Locate every blood parasite and identify its species.
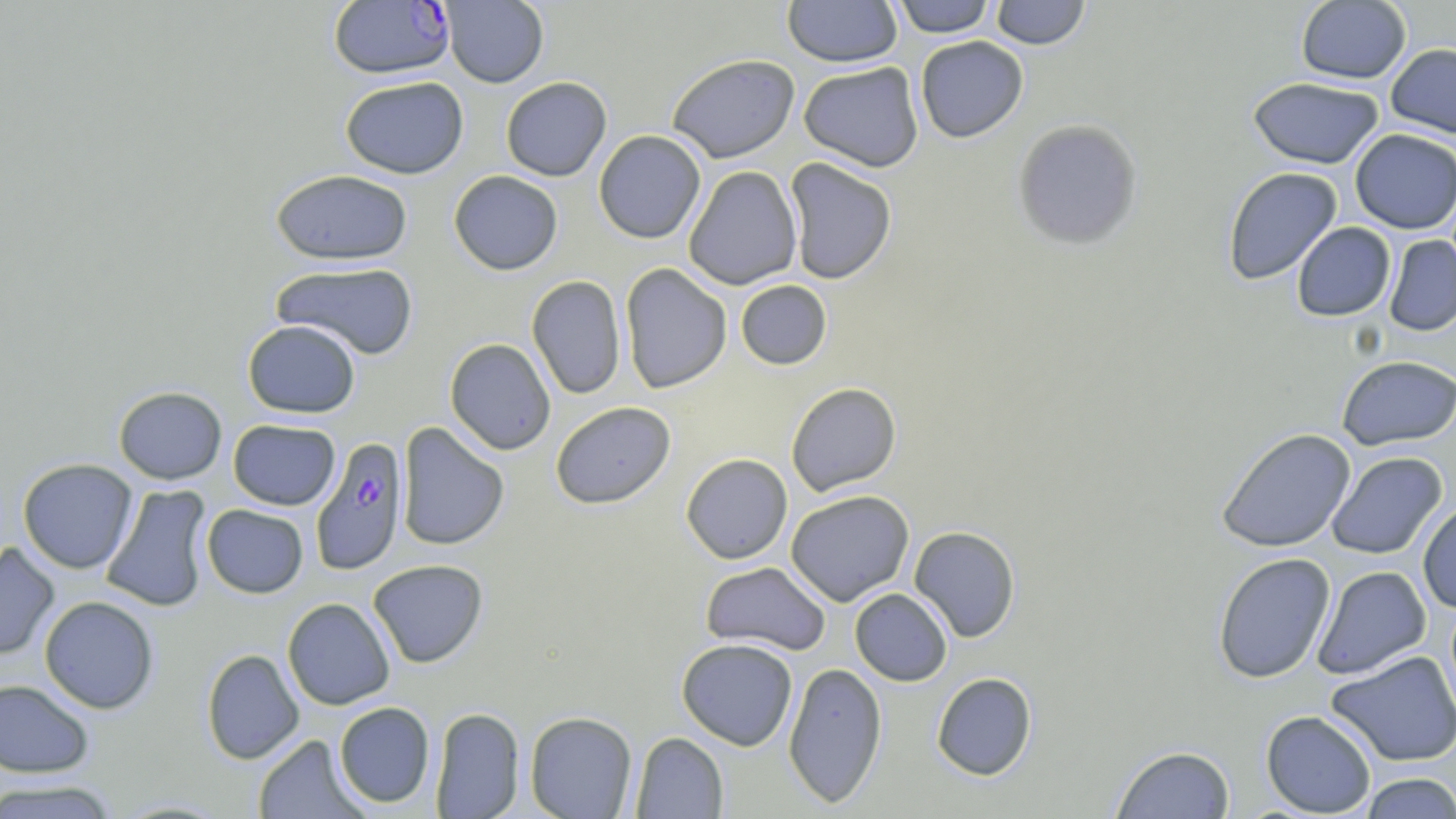

Approximate bounding boxes as [x1, y1, x2, y2] in pixels.
Plasmodium falciparum-infected red blood cells: [328, 1, 455, 79], [310, 436, 409, 575].
No Plasmodium ovale, Plasmodium malariae, Plasmodium vivax, Babesia divergens, or Trypanosoma brucei observed.

Summary:
  - Uninfected red blood cell locations: [440, 0, 549, 88], [782, 0, 902, 67], [890, 0, 996, 37], [990, 0, 1090, 49], [1296, 1, 1411, 84], [915, 36, 1028, 143], [1385, 43, 1456, 139], [666, 53, 800, 163], [798, 62, 924, 172], [340, 76, 469, 179], [500, 76, 612, 181], [1247, 77, 1385, 169], [1012, 118, 1143, 250], [1350, 128, 1456, 234], [593, 130, 706, 244], [784, 157, 898, 285], [683, 165, 802, 290], [1222, 167, 1343, 285], [271, 169, 414, 265], [448, 170, 563, 275], [1291, 222, 1395, 321], [1384, 235, 1456, 336], [270, 261, 419, 359], [619, 263, 733, 394], [527, 275, 626, 400], [735, 280, 832, 370], [243, 319, 360, 418], [445, 338, 556, 455], [1337, 354, 1456, 451], [786, 382, 902, 496], [113, 385, 227, 484], [550, 401, 676, 509], [228, 419, 340, 510], [396, 421, 509, 551], [1216, 427, 1356, 553], [1326, 451, 1448, 560], [681, 453, 793, 564], [17, 458, 138, 573], [100, 484, 213, 613], [785, 490, 914, 606], [1417, 501, 1456, 613], [202, 504, 308, 598], [909, 526, 1021, 642], [0, 541, 60, 662], [1212, 552, 1336, 684], [368, 559, 489, 668], [700, 561, 831, 656], [1312, 565, 1432, 680], [850, 588, 953, 686], [39, 596, 159, 714], [282, 597, 395, 710], [676, 639, 799, 750], [201, 648, 304, 764], [1325, 650, 1456, 767], [783, 661, 888, 808], [931, 671, 1037, 781], [0, 679, 95, 778], [334, 701, 435, 808], [429, 707, 525, 818], [1260, 710, 1377, 817], [525, 711, 637, 819], [630, 732, 728, 818], [253, 733, 369, 819], [1110, 744, 1236, 818], [1357, 772, 1456, 818], [0, 778, 121, 818]
  - Slide-level diagnosis: Plasmodium falciparum
  - Image size: 1456×819 pixels
  - Magnification: 1000x
  - Stain: May-Grünwald-Giemsa
  - Field of view: single
  - Preparation: thin blood smear
  - Modality: light microscopy